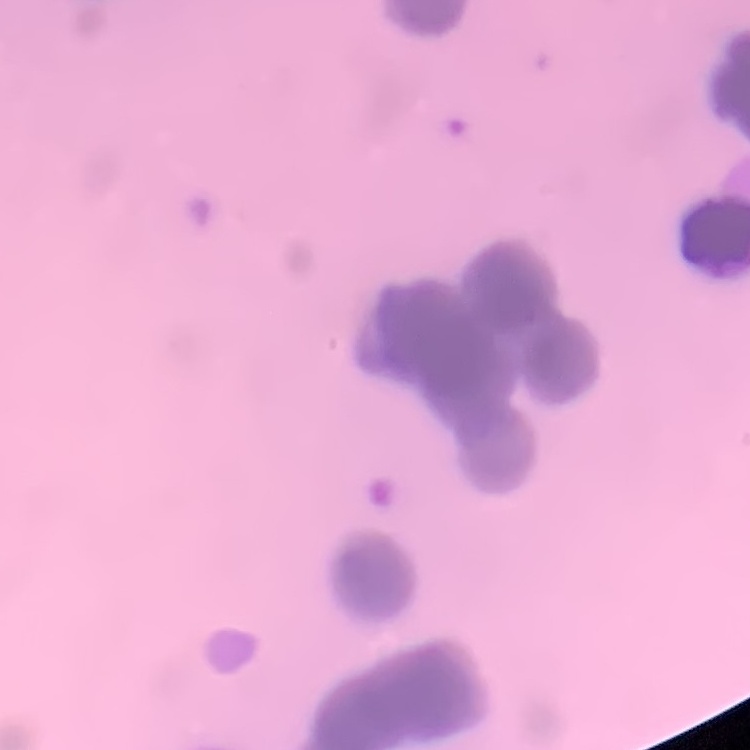 The erythrocytes exhibit rouleaux formation. Square crop of a larger photomicrograph. Thin peripheral smear. Stained with either Field's or Giemsa.